Report the malaria status of this cell.
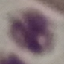
Uninfected.

Summary:
  - Preparation: thin blood film
  - Image type: cell patch, automatically extracted from a larger field of view and resized to 64 × 64 pixels
  - Stain: Giemsa
  - Capture: smartphone camera at the microscope eyepiece